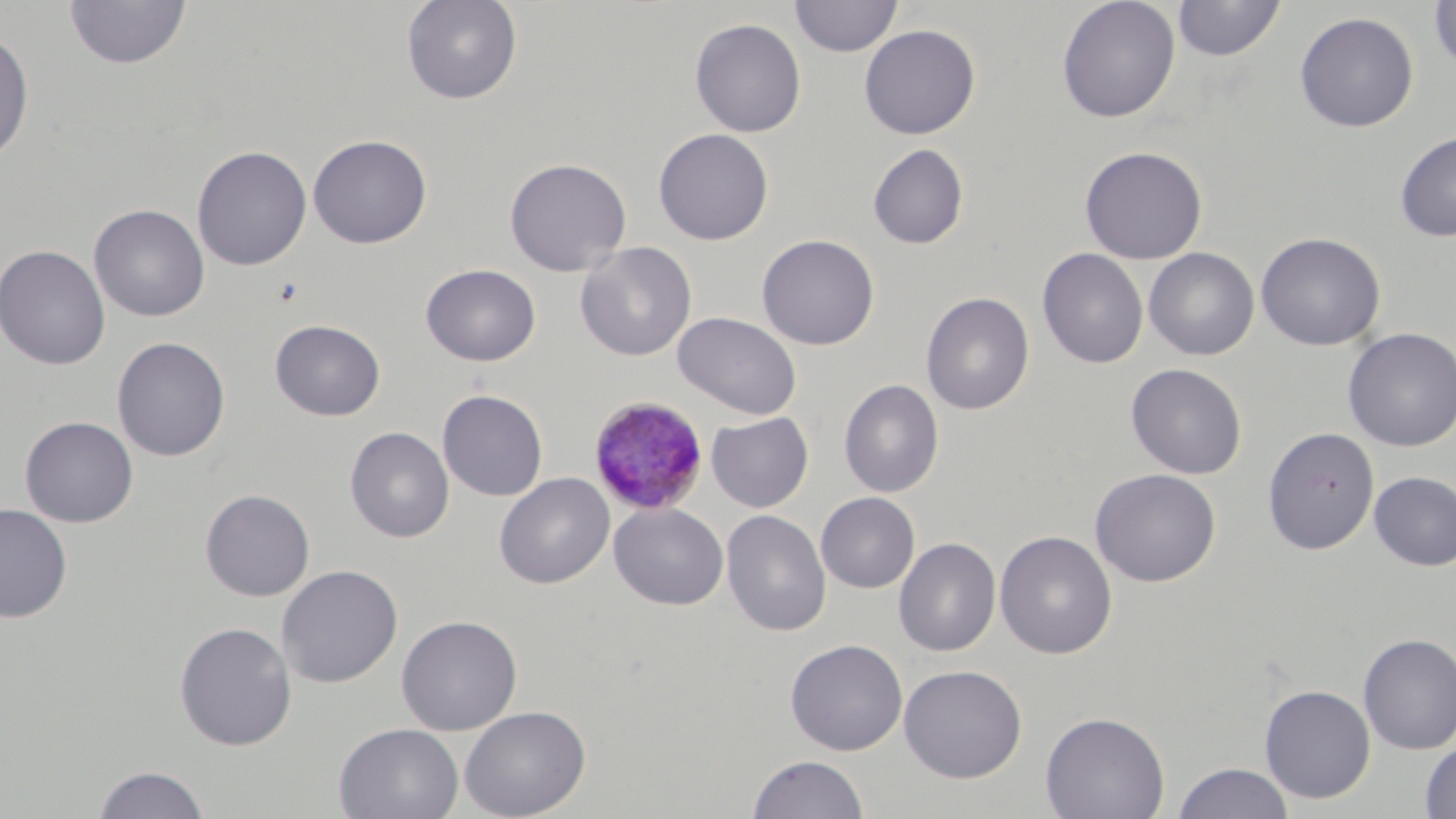

slide-level diagnosis = Plasmodium malariae
field of view = single
magnification = 1000x
uninfected red blood cell locations = approximate bounding boxes as named x1/y1/x2/y2 corners in pixels: (x1=400, y1=0, x2=523, y2=105), (x1=790, y1=0, x2=902, y2=57), (x1=1057, y1=0, x2=1181, y2=123), (x1=1173, y1=0, x2=1286, y2=61), (x1=64, y1=1, x2=191, y2=70), (x1=1428, y1=1, x2=1456, y2=74), (x1=1295, y1=11, x2=1418, y2=133), (x1=689, y1=18, x2=806, y2=138), (x1=859, y1=24, x2=980, y2=139), (x1=0, y1=29, x2=34, y2=167), (x1=653, y1=128, x2=774, y2=245), (x1=1394, y1=130, x2=1456, y2=242), (x1=307, y1=134, x2=432, y2=249), (x1=867, y1=143, x2=969, y2=250), (x1=192, y1=145, x2=312, y2=271), (x1=1080, y1=146, x2=1207, y2=264), (x1=504, y1=157, x2=631, y2=277), (x1=89, y1=203, x2=209, y2=322), (x1=1256, y1=232, x2=1385, y2=351), (x1=757, y1=234, x2=879, y2=350), (x1=575, y1=242, x2=697, y2=361), (x1=0, y1=243, x2=110, y2=370), (x1=1144, y1=247, x2=1260, y2=361), (x1=1038, y1=248, x2=1148, y2=369), (x1=420, y1=263, x2=541, y2=366), (x1=921, y1=292, x2=1035, y2=415), (x1=673, y1=312, x2=801, y2=419), (x1=270, y1=319, x2=386, y2=421), (x1=1343, y1=327, x2=1456, y2=451), (x1=112, y1=336, x2=230, y2=461), (x1=1126, y1=363, x2=1248, y2=479), (x1=839, y1=378, x2=944, y2=498), (x1=436, y1=389, x2=548, y2=501), (x1=706, y1=412, x2=813, y2=512), (x1=19, y1=416, x2=139, y2=527), (x1=345, y1=426, x2=454, y2=543), (x1=1262, y1=427, x2=1379, y2=554), (x1=1090, y1=468, x2=1221, y2=587), (x1=1369, y1=471, x2=1456, y2=571), (x1=494, y1=472, x2=615, y2=589), (x1=200, y1=489, x2=315, y2=601), (x1=815, y1=492, x2=920, y2=593), (x1=608, y1=502, x2=728, y2=610), (x1=0, y1=504, x2=73, y2=622), (x1=721, y1=509, x2=832, y2=636), (x1=995, y1=530, x2=1117, y2=659), (x1=894, y1=537, x2=1002, y2=656), (x1=276, y1=564, x2=403, y2=688), (x1=396, y1=614, x2=522, y2=735), (x1=174, y1=621, x2=297, y2=750), (x1=1358, y1=633, x2=1456, y2=754), (x1=785, y1=638, x2=908, y2=755), (x1=898, y1=664, x2=1027, y2=782), (x1=1260, y1=684, x2=1375, y2=803), (x1=459, y1=704, x2=591, y2=819), (x1=1040, y1=711, x2=1170, y2=819), (x1=333, y1=723, x2=464, y2=819), (x1=1419, y1=739, x2=1456, y2=818), (x1=747, y1=754, x2=868, y2=819), (x1=1172, y1=762, x2=1295, y2=819), (x1=92, y1=764, x2=212, y2=819)
preparation = thin blood smear
modality = optical microscopy
stain = May-Grünwald-Giemsa
image size = 1456×819 pixels
Plasmodium malariae-infected red blood cell locations = approximate bounding boxes as named x1/y1/x2/y2 corners in pixels: (x1=589, y1=396, x2=709, y2=515)